Classify this cell by malaria status.
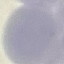
It is uninfected.

Thin blood smear. Acquired by smartphone through the microscope eyepiece. Automatically extracted cell patch, resized to 64 × 64 pixels. Giemsa-stained preparation.